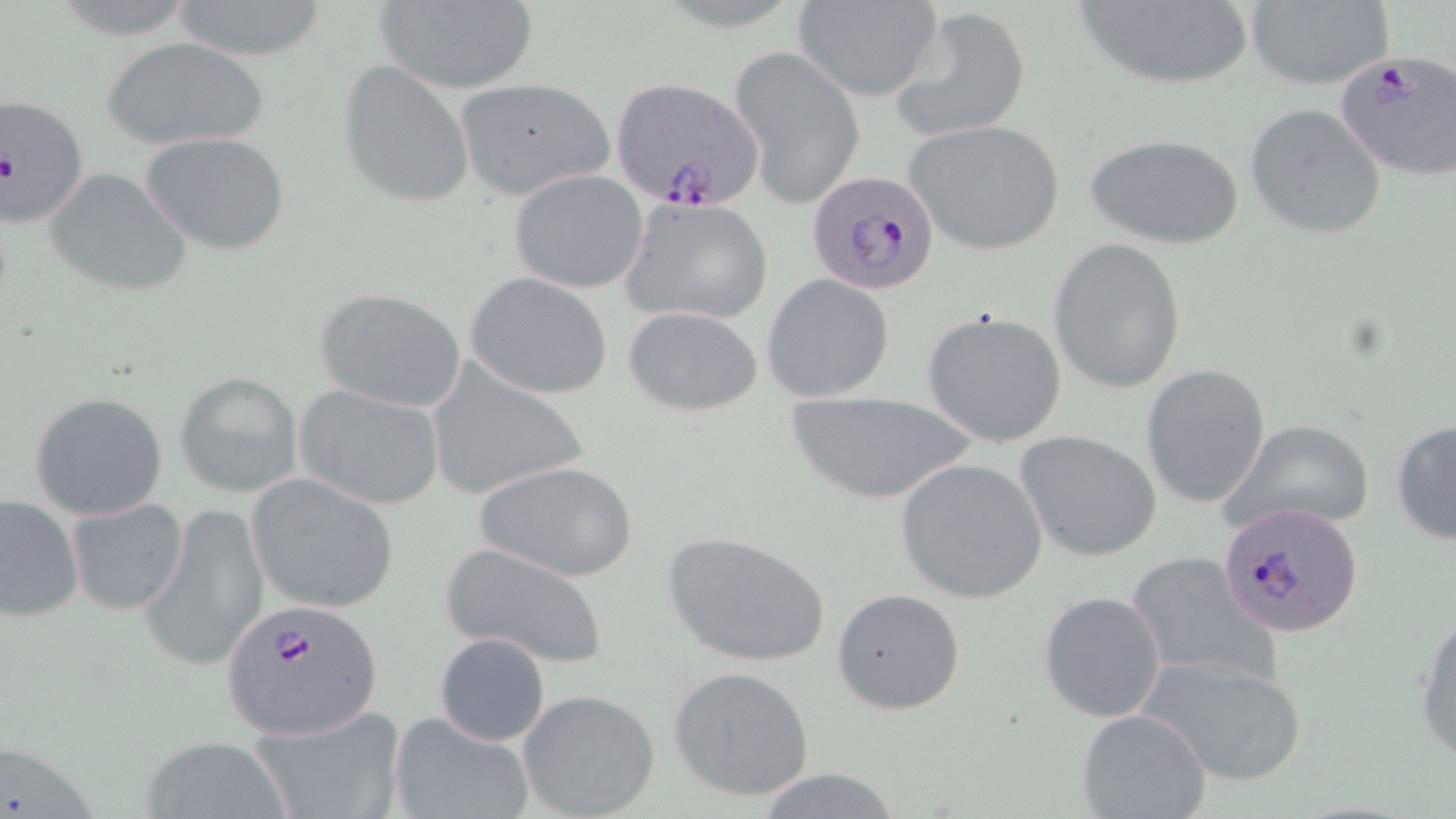
Approximate bounding boxes as [x1, y1, x2, y2] in pixels. Plasmodium falciparum-infected red blood cell locations: [1333, 51, 1456, 180], [609, 76, 764, 211], [806, 168, 940, 296], [1220, 503, 1365, 637], [224, 599, 384, 739]. Uninfected red blood cell locations: [370, 0, 539, 93], [792, 0, 943, 102], [1074, 0, 1252, 93], [166, 1, 333, 61], [1243, 1, 1394, 90], [888, 7, 1032, 140], [99, 35, 271, 152], [729, 47, 867, 208], [337, 61, 478, 208], [454, 78, 614, 201], [2, 92, 94, 227], [1244, 102, 1388, 241], [903, 117, 1067, 256], [141, 131, 291, 256], [1083, 131, 1245, 250], [44, 166, 193, 298], [509, 169, 649, 293], [622, 196, 773, 325], [1049, 239, 1187, 394], [463, 271, 615, 400], [761, 274, 896, 404], [313, 287, 467, 413], [622, 304, 764, 417], [920, 310, 1068, 448], [425, 363, 593, 501], [1140, 363, 1272, 510], [175, 371, 304, 498], [293, 384, 446, 510], [29, 390, 168, 521], [783, 390, 977, 506], [1390, 415, 1456, 547], [1222, 419, 1375, 535], [1016, 429, 1163, 562], [896, 458, 1048, 603], [472, 459, 640, 583], [246, 474, 401, 614], [0, 492, 84, 624], [66, 498, 189, 614], [141, 501, 270, 675], [661, 531, 833, 669], [439, 541, 610, 671], [1127, 549, 1279, 690], [831, 586, 966, 715], [1037, 590, 1167, 723], [1412, 608, 1456, 768], [434, 631, 551, 746], [1138, 652, 1309, 786], [668, 665, 816, 802], [518, 688, 662, 819], [248, 705, 407, 819], [1077, 708, 1212, 819], [390, 709, 536, 819], [139, 734, 292, 819], [748, 770, 907, 819]. Slide-level diagnosis: Plasmodium falciparum. Single field of view. May-Grünwald-Giemsa-stained preparation. Captured at 1000x magnification. Image is 1456×819 pixels. Thin blood film. Light microscopy.